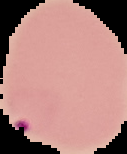

Summary:
  - Image type: cell region segmented out of the field of view; surrounding area masked to black
  - Image size: 127×154 pixels
  - Result: Plasmodium parasites detected
  - Preparation: thin blood film